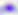

Toxoplasma gondii is shown. 400x magnification. Micrograph.